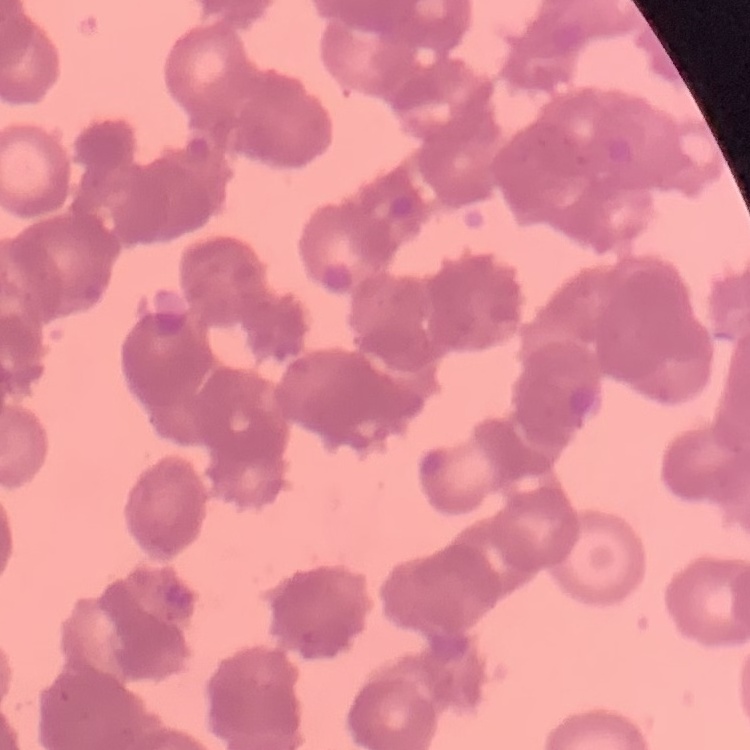
erythrocyte morphology = rouleaux formation
stain = Field's or Giemsa
image type = square crop of a larger photomicrograph
preparation = thin peripheral smear